Report the malaria status of this cell.
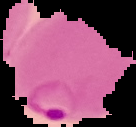

It is parasitized.

Image is 136×127 pixels. From a thin blood film. The area outside the segmented cell region is set to black.